Identify the parasite.
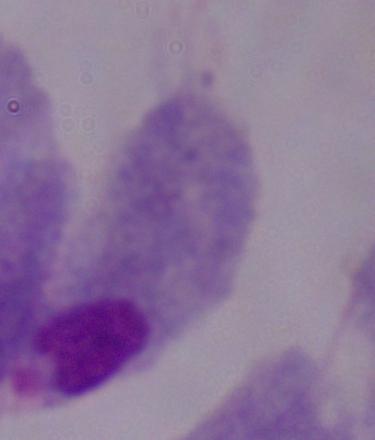

This is a trichomonad.

1000x magnification. Photomicrograph.